Assess this cell for malaria.
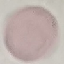

It is uninfected.

Summary:
  - Stain: Giemsa
  - Preparation: thin smear
  - Image type: automatically extracted cell patch, resized to 64 × 64 pixels
  - Capture: smartphone camera at the microscope eyepiece